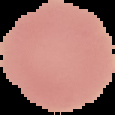
Summary:
  - Image size: 115×115 pixels
  - Image type: segmented cell region with the area outside set to black
  - Preparation: thin blood film
  - Malaria status: uninfected